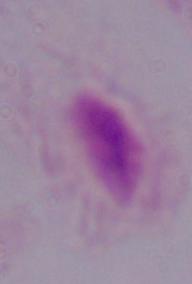
magnification = 1000x
identification = trichomonad
modality = photomicrograph